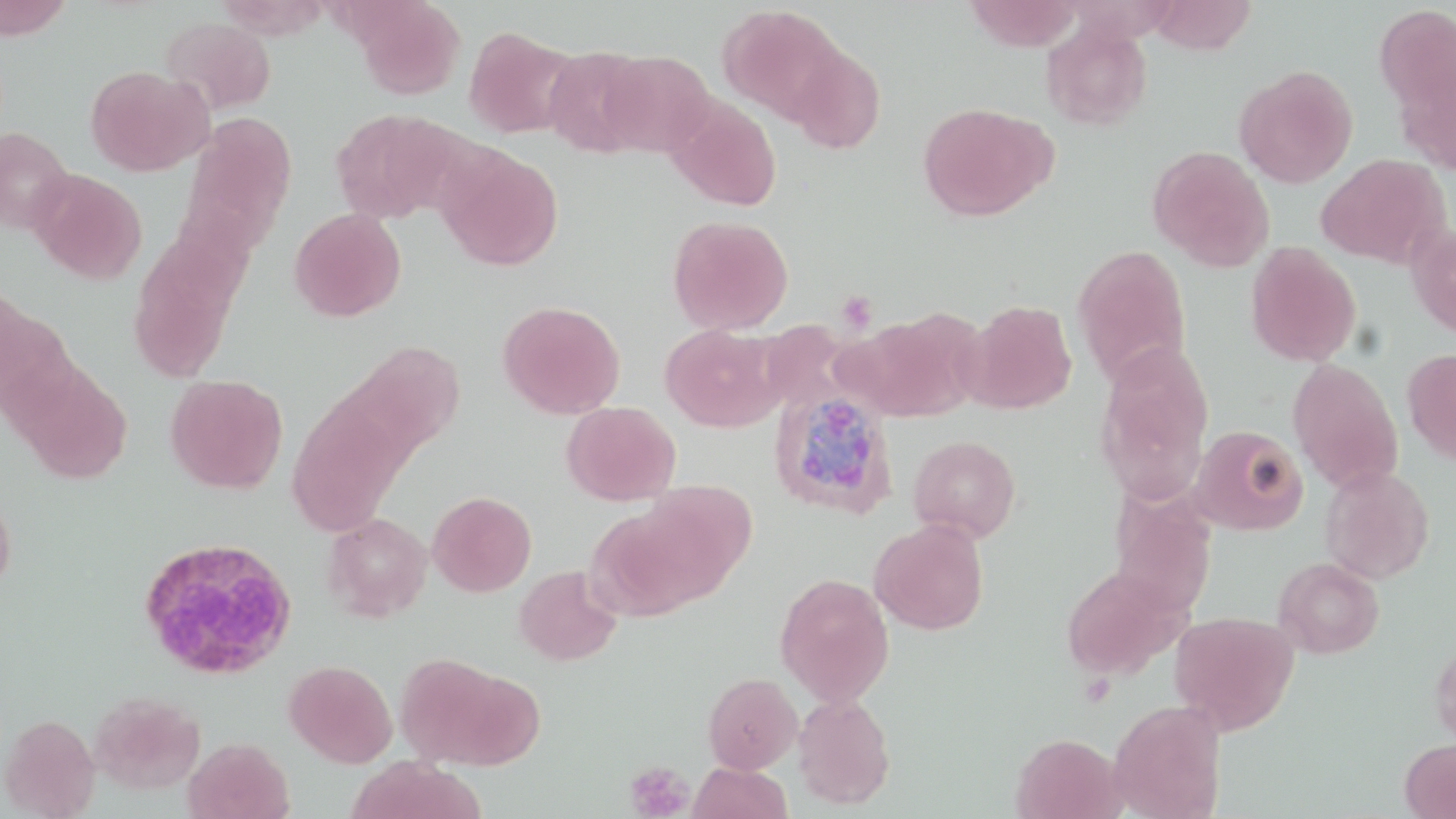

Summary:
  - Coordinate format: approximate bounding boxes as [x1, y1, x2, y2] in pixels
  - White blood cell locations: [137, 536, 298, 680]
  - Plasmodium ovale-infected red blood cell locations: [768, 388, 899, 519]
  - Uninfected red blood cell locations: [0, 0, 73, 39], [352, 0, 465, 100], [963, 0, 1086, 50], [1145, 0, 1257, 55], [1373, 4, 1456, 122], [717, 5, 848, 125], [161, 16, 277, 116], [1041, 19, 1152, 131], [464, 25, 579, 139], [541, 46, 654, 157], [788, 46, 887, 156], [598, 50, 717, 157], [1391, 53, 1456, 176], [1233, 64, 1358, 188], [84, 66, 213, 176], [665, 96, 782, 212], [916, 102, 1054, 222], [331, 108, 458, 224], [184, 112, 297, 243], [0, 125, 73, 234], [434, 144, 564, 271], [1148, 145, 1275, 272], [1316, 153, 1450, 269], [29, 169, 147, 284], [289, 208, 406, 322], [666, 214, 794, 335], [1405, 222, 1456, 340], [128, 232, 243, 383], [1245, 242, 1362, 367], [1072, 243, 1192, 388], [0, 296, 76, 428], [963, 299, 1077, 414], [497, 301, 625, 418], [842, 311, 980, 422], [660, 324, 785, 432], [355, 341, 466, 455], [1094, 345, 1214, 502], [1402, 347, 1456, 465], [1287, 358, 1404, 494], [13, 362, 133, 484], [165, 374, 288, 494], [287, 395, 407, 534], [561, 402, 681, 506], [1190, 425, 1309, 536], [908, 434, 1021, 542], [1320, 466, 1436, 585], [628, 480, 757, 607], [427, 491, 537, 596], [0, 492, 16, 597], [322, 512, 433, 621], [869, 518, 990, 635], [1273, 556, 1385, 659], [1061, 564, 1187, 680], [513, 565, 623, 666], [774, 572, 895, 707], [1169, 610, 1299, 735], [1428, 634, 1456, 749], [394, 654, 523, 768], [283, 659, 398, 768], [703, 672, 802, 773], [89, 691, 206, 795], [793, 693, 896, 809], [1107, 699, 1227, 819], [0, 713, 100, 818], [1011, 732, 1125, 819], [182, 737, 294, 819], [1399, 738, 1456, 818], [347, 758, 481, 819], [687, 762, 792, 819]
  - Platelet locations: [836, 290, 878, 335], [624, 761, 694, 818]
  - Slide-level diagnosis: Plasmodium ovale
  - Image size: 1456×819 pixels
  - Magnification: 1000x
  - Preparation: thin blood smear
  - Modality: optical microscopy
  - Stain: May-Grünwald-Giemsa
  - Field of view: one of a larger specimen